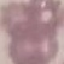 Malaria status: uninfected. Automatically extracted cell patch, resized to 64 × 64 pixels. Thin blood smear. Giemsa stain. Acquired by smartphone through the microscope eyepiece.